Assess this cell for malaria.
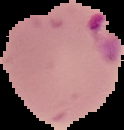

It is parasitized.

image type = cell region segmented out of the field of view; surrounding area masked to black
image size = 124×130 pixels
preparation = thin blood smear